Locate and identify every blood parasite.
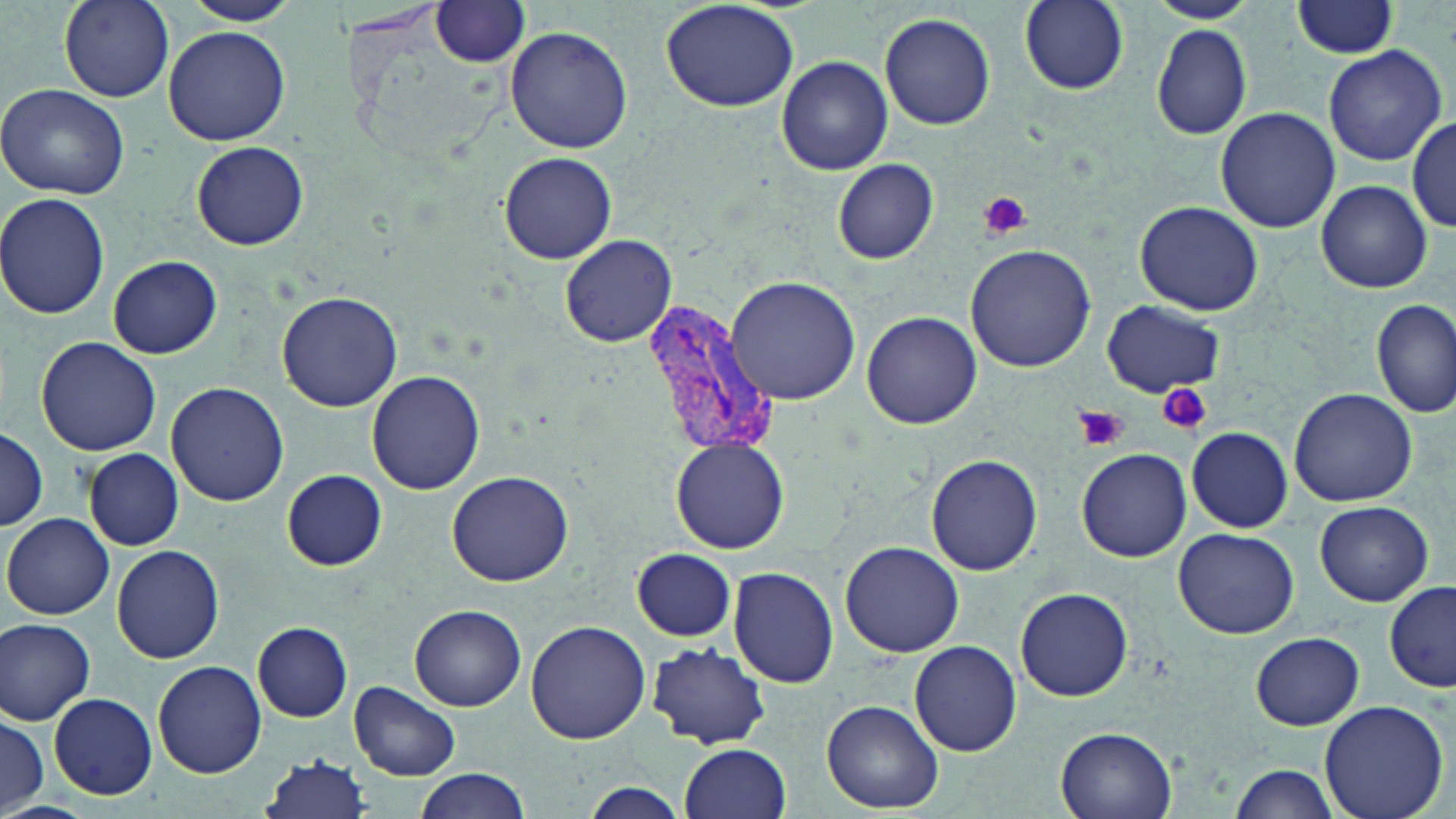
Approximate bounding boxes as (x1,y1)-(x2,y2) corner pairs in pixels.
Plasmodium vivax-infected red blood cells: (640,293)-(777,460).
No Plasmodium falciparum, Plasmodium ovale, Plasmodium malariae, Babesia divergens, or Trypanosoma brucei observed.

Summary:
  - Platelet locations: (977,190)-(1032,241), (1157,384)-(1212,437), (1074,405)-(1129,454)
  - Uninfected red blood cell locations: (59,0)-(176,103), (181,0)-(301,25), (661,0)-(801,114), (1019,0)-(1130,94), (1146,0)-(1261,24), (428,1)-(533,68), (1293,1)-(1401,59), (880,12)-(997,130), (163,25)-(291,146), (505,25)-(633,154), (1151,25)-(1253,139), (1321,45)-(1448,167), (776,56)-(892,175), (0,84)-(132,200), (1215,107)-(1341,232), (1407,118)-(1456,232), (192,140)-(309,250), (499,152)-(619,265), (832,159)-(940,264), (1316,181)-(1432,293), (0,193)-(114,320), (1134,201)-(1263,315), (560,234)-(676,348), (964,243)-(1096,373), (108,255)-(222,358), (725,277)-(863,405), (277,289)-(403,411), (1372,299)-(1455,420), (1102,301)-(1225,397), (861,310)-(982,428), (35,337)-(165,457), (367,371)-(486,496), (166,381)-(290,505), (1289,388)-(1418,506), (1186,426)-(1294,532), (0,428)-(48,531), (670,438)-(791,554), (1076,448)-(1192,562), (84,449)-(184,550), (925,454)-(1043,576), (281,469)-(387,569), (446,469)-(574,587), (1315,501)-(1433,606), (3,512)-(115,619), (1173,527)-(1299,640), (842,541)-(963,657), (113,544)-(225,663), (632,549)-(737,642), (728,567)-(839,688), (1385,581)-(1455,692), (1016,587)-(1134,701), (410,605)-(525,711), (1,618)-(97,725), (525,621)-(651,744), (252,622)-(354,722), (1251,632)-(1365,730), (909,640)-(1022,757), (646,643)-(772,747), (153,661)-(266,777), (349,680)-(462,782), (48,694)-(156,798), (1318,698)-(1451,819), (822,700)-(944,814), (0,715)-(48,816), (1056,726)-(1178,819), (679,743)-(791,819), (259,755)-(373,819), (1229,760)-(1344,818), (411,769)-(531,819), (580,782)-(687,819), (0,802)-(97,819)
  - Slide-level diagnosis: Plasmodium vivax
  - Magnification: 1000x
  - Field of view: single
  - Modality: optical microscopy
  - Image size: 1456×819 pixels
  - Preparation: thin blood smear
  - Stain: May-Grünwald-Giemsa